Assess this cell for malaria.
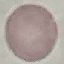

It is uninfected.

Cell patch, automatically extracted from a larger field of view and resized to 64 × 64 pixels. Thin blood film. Giemsa stain. Acquired by smartphone through the microscope eyepiece.